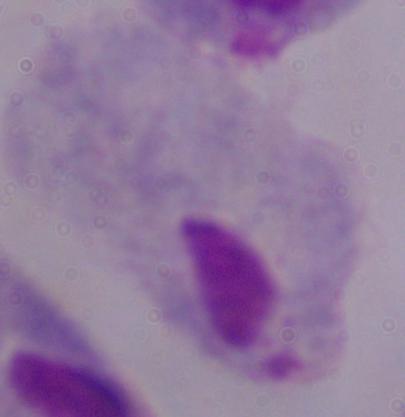

Captured at 1000x magnification. A trichomonad is seen. Photomicrograph.